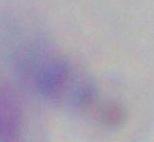

Summary:
  - Magnification: 1000x
  - Identification: Toxoplasma gondii
  - Modality: photomicrograph